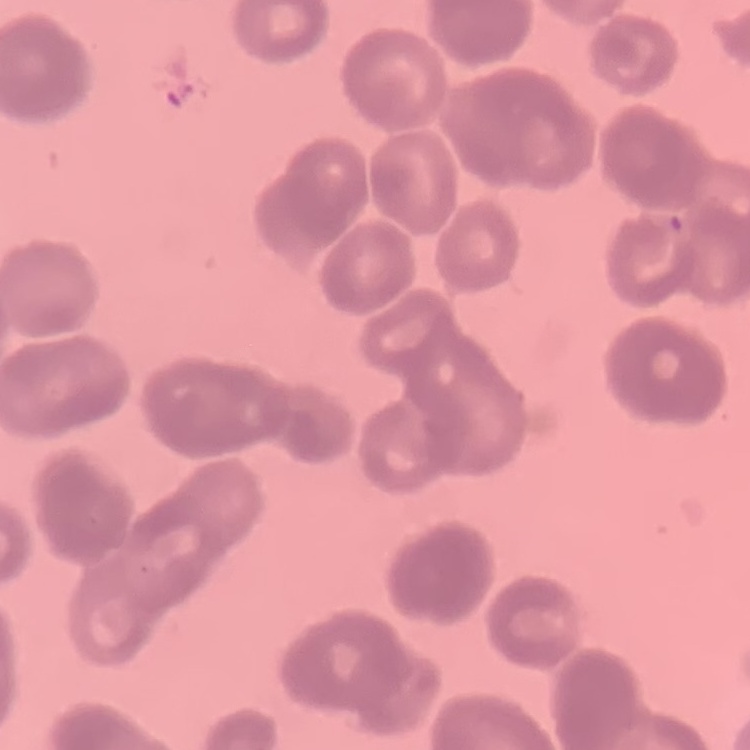

Summary:
  - Erythrocyte morphology: rouleaux formation
  - Preparation: thin blood film
  - Stain: Field's or Giemsa
  - Image type: one tile cut from a larger photomicrograph